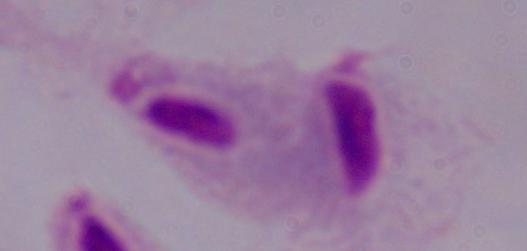 Captured at 1000x magnification. Photomicrograph. A trichomonad is shown.